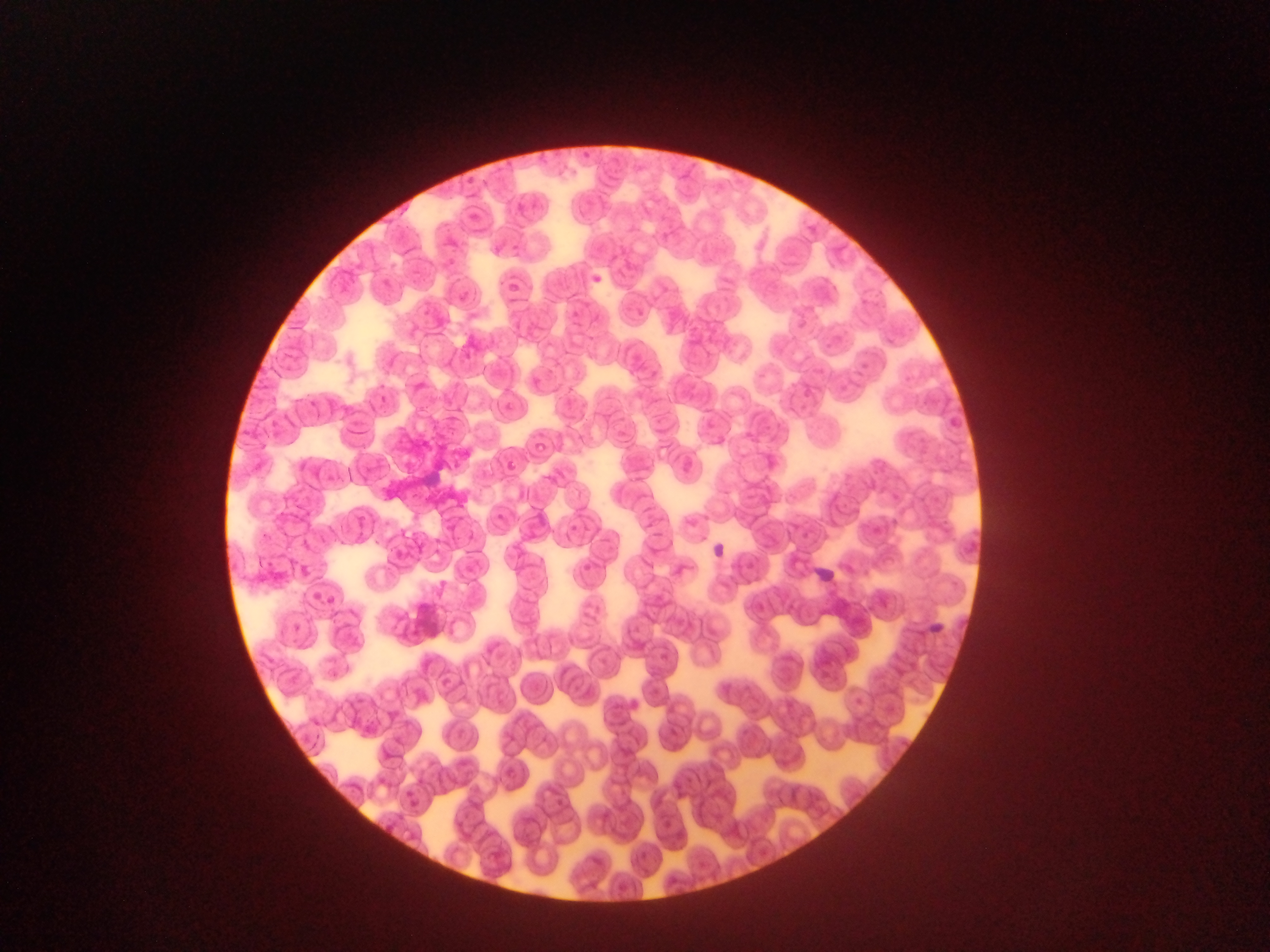

{
  "image_size": "1270×952 pixels",
  "preparation": "thin blood smear",
  "capture": "mobile-phone photograph through a microscope",
  "country": "Ghana",
  "malaria_parasite_locations": "approximate bounding boxes as [left, top, right, bottom] in pixels: [498, 399, 518, 417], [500, 457, 519, 475], [402, 790, 421, 809]",
  "field_of_view": "single"
}